Locate every Plasmodium ovale-infected red blood cell.
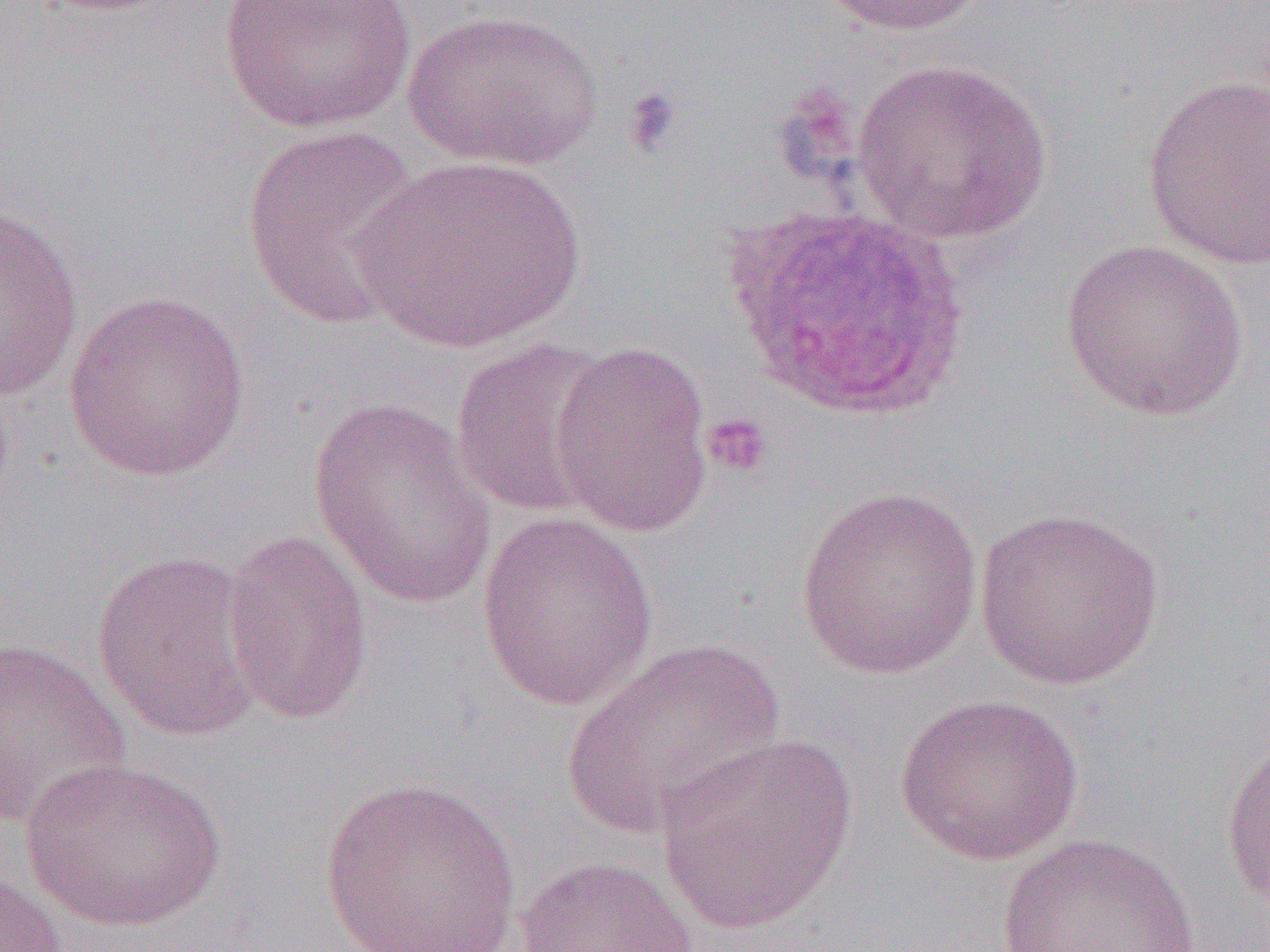
Approximate bounding boxes as (x1,y1)-(x2,y2) corner pairs in pixels.
Plasmodium ovale-infected red blood cells: (723,205)-(973,424).

slide-level diagnosis = Plasmodium ovale
image size = 1270×952 pixels
field of view = single
magnification = 1000x
uninfected red blood cell locations = approximate bounding boxes as (x1,y1)-(x2,y2) corner pairs in pixels: (217,0)-(416,135), (816,0)-(986,36), (401,8)-(603,171), (848,57)-(1054,246), (1141,72)-(1270,270), (241,124)-(423,331), (354,154)-(585,352), (0,205)-(84,401), (1059,239)-(1248,421), (61,289)-(253,483), (449,338)-(619,519), (550,339)-(715,536), (308,400)-(498,610), (795,484)-(984,679), (973,507)-(1166,690), (476,512)-(658,710), (220,528)-(373,726), (90,549)-(266,744), (0,637)-(131,833), (562,638)-(783,839), (893,692)-(1085,865), (653,733)-(857,934), (1220,736)-(1270,921), (19,757)-(227,932), (319,776)-(522,951), (995,832)-(1202,951), (513,855)-(701,952), (0,868)-(73,951)
platelet locations = approximate bounding boxes as (x1,y1)-(x2,y2) corner pairs in pixels: (621,86)-(684,157), (702,412)-(774,478)
modality = light microscopy
preparation = thin blood film